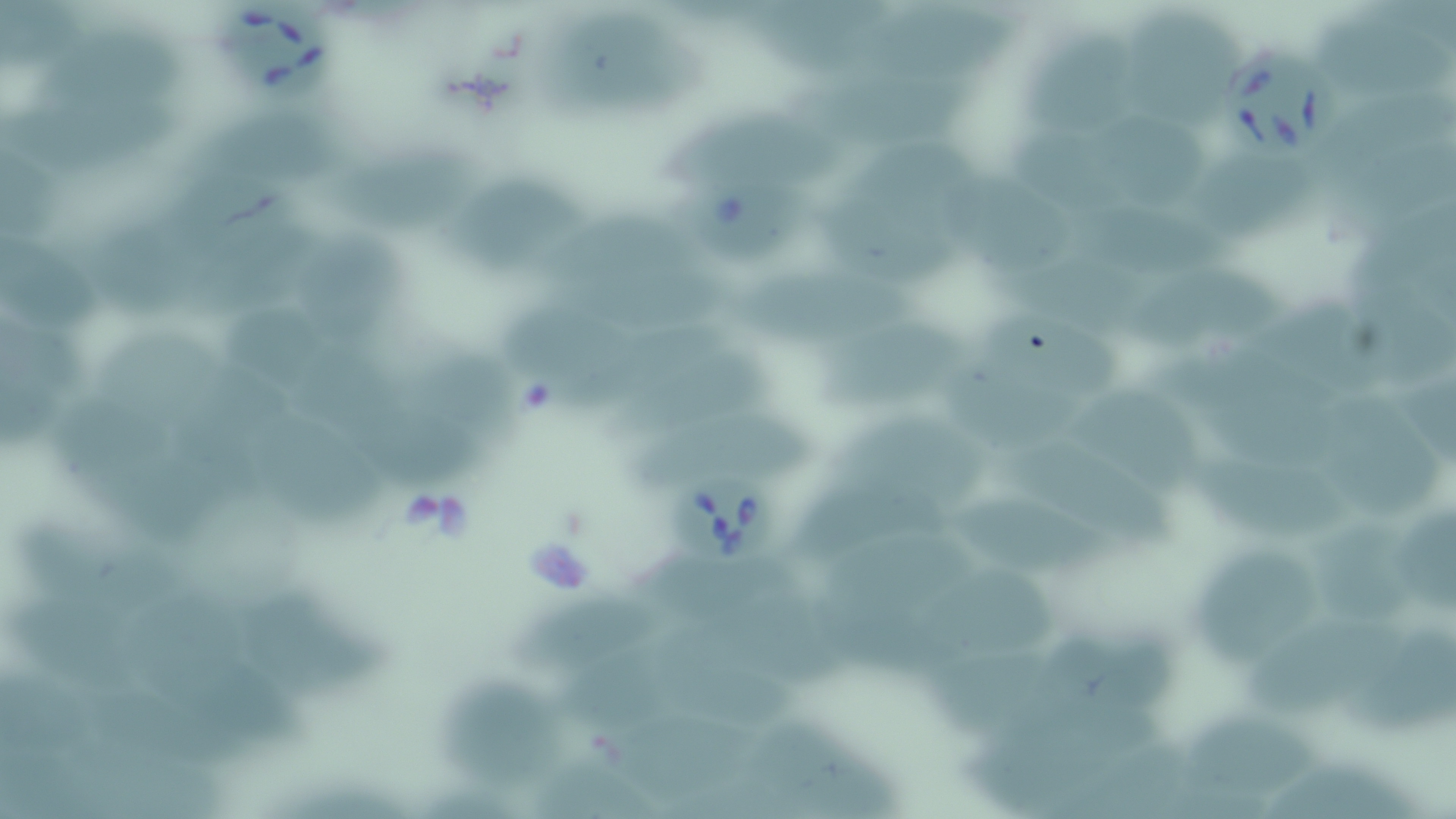
Approximate bounding boxes as (x1,y1)-(x2,y2) corner pairs in pixels. Uninfected red blood cell locations: (4,3)-(92,65), (748,6)-(887,76), (1130,9)-(1247,119), (882,10)-(1014,82), (567,14)-(711,115), (1318,21)-(1451,96), (1019,29)-(1136,131), (40,47)-(186,107), (803,73)-(979,145), (1330,90)-(1453,175), (8,92)-(188,164), (200,105)-(335,192), (669,108)-(847,188), (1109,116)-(1212,210), (1015,119)-(1127,210), (835,133)-(1001,208), (327,147)-(481,222), (1333,147)-(1455,234), (1204,153)-(1323,233), (170,156)-(276,242), (13,165)-(63,239), (449,174)-(590,269), (949,177)-(1075,274), (822,195)-(953,283), (1345,198)-(1456,314), (548,211)-(720,281), (1094,211)-(1237,282), (206,214)-(330,317), (106,228)-(202,317), (303,228)-(406,338), (4,232)-(98,329), (999,247)-(1170,316), (736,266)-(924,341), (1140,267)-(1272,351), (560,269)-(727,328), (1374,286)-(1456,380), (503,293)-(658,393), (993,305)-(1125,392), (1262,306)-(1385,395), (229,307)-(350,391), (823,316)-(975,411), (560,318)-(739,414), (4,324)-(114,381), (105,330)-(243,410), (304,348)-(406,436), (613,352)-(774,436), (1173,352)-(1350,422), (410,353)-(519,455), (952,356)-(1071,434), (176,365)-(294,466), (5,369)-(62,451), (1075,384)-(1197,491), (64,388)-(196,477), (1331,396)-(1440,515), (371,401)-(480,489), (631,406)-(833,490), (1204,407)-(1351,471), (268,417)-(393,530), (838,421)-(996,505), (1026,440)-(1185,537), (1188,456)-(1358,541), (963,490)-(1125,578), (802,491)-(952,566), (1404,502)-(1456,615), (21,514)-(193,608), (1323,523)-(1420,633), (827,530)-(985,597), (633,546)-(795,627), (1199,546)-(1327,668), (719,588)-(861,690), (971,589)-(1062,650), (143,591)-(249,722), (524,592)-(669,670), (255,593)-(398,710), (6,595)-(149,701), (1248,612)-(1406,725), (1349,625)-(1456,739), (933,640)-(1058,731), (567,648)-(680,730), (1064,651)-(1176,734), (677,660)-(791,734), (206,665)-(314,747), (448,672)-(570,785), (105,683)-(248,776), (606,703)-(759,790), (956,707)-(1162,806), (1186,710)-(1330,800), (752,719)-(886,798), (71,747)-(249,814), (521,749)-(650,819), (1266,759)-(1425,819), (426,781)-(525,819). Babesia divergens-infected red blood cell locations: (213,5)-(336,107), (1224,49)-(1338,163), (680,180)-(814,262), (669,480)-(784,574). Slide-level diagnosis: Babesia divergens. Captured at 1000x magnification. Image is 1456×819 pixels. May-Grünwald-Giemsa-stained preparation. Thin blood smear. One field of a larger specimen. Light microscopy.